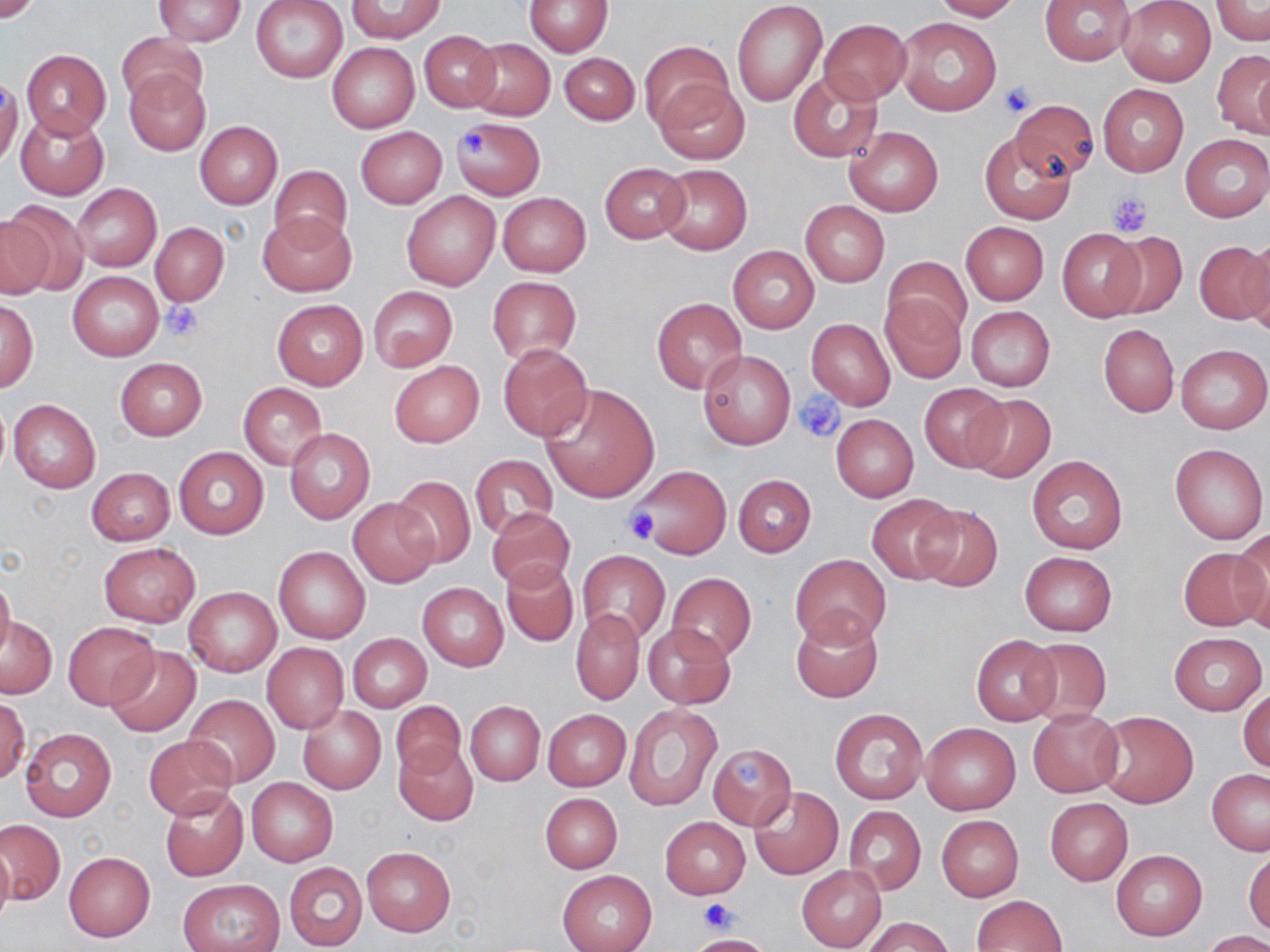
{
  "slide_level_diagnosis": "no evidence of blood parasites",
  "modality": "light microscopy",
  "image_size": "1270×952 pixels",
  "preparation": "thin blood film",
  "platelet_locations": "approximate bounding boxes as named x1/y1/x2/y2 corners in pixels: (x1=998, y1=80, x2=1038, y2=118), (x1=460, y1=130, x2=489, y2=156), (x1=1108, y1=191, x2=1153, y2=236), (x1=161, y1=300, x2=203, y2=341), (x1=796, y1=392, x2=845, y2=443), (x1=621, y1=507, x2=660, y2=546), (x1=733, y1=754, x2=761, y2=784), (x1=699, y1=898, x2=736, y2=934)",
  "uninfected_red_blood_cell_locations": "approximate bounding boxes as named x1/y1/x2/y2 corners in pixels: (x1=0, y1=0, x2=44, y2=23), (x1=251, y1=0, x2=347, y2=82), (x1=524, y1=0, x2=611, y2=56), (x1=733, y1=0, x2=828, y2=107), (x1=929, y1=0, x2=1021, y2=21), (x1=1039, y1=0, x2=1137, y2=65), (x1=153, y1=1, x2=247, y2=46), (x1=346, y1=1, x2=448, y2=42), (x1=1118, y1=1, x2=1215, y2=86), (x1=1210, y1=1, x2=1270, y2=44), (x1=895, y1=17, x2=1001, y2=117), (x1=819, y1=19, x2=911, y2=103), (x1=418, y1=30, x2=501, y2=111), (x1=116, y1=32, x2=205, y2=109), (x1=467, y1=38, x2=555, y2=121), (x1=641, y1=41, x2=732, y2=128), (x1=326, y1=42, x2=420, y2=133), (x1=1211, y1=49, x2=1270, y2=137), (x1=22, y1=50, x2=111, y2=138), (x1=560, y1=53, x2=640, y2=124), (x1=124, y1=68, x2=211, y2=156), (x1=787, y1=69, x2=884, y2=162), (x1=0, y1=75, x2=22, y2=168), (x1=654, y1=80, x2=750, y2=166), (x1=1097, y1=83, x2=1188, y2=177), (x1=1010, y1=99, x2=1099, y2=180), (x1=15, y1=110, x2=110, y2=200), (x1=450, y1=117, x2=546, y2=200), (x1=194, y1=121, x2=282, y2=208), (x1=845, y1=125, x2=943, y2=216), (x1=355, y1=126, x2=447, y2=208), (x1=980, y1=131, x2=1075, y2=224), (x1=1180, y1=134, x2=1270, y2=222), (x1=599, y1=162, x2=690, y2=243), (x1=657, y1=164, x2=751, y2=255), (x1=269, y1=165, x2=352, y2=247), (x1=73, y1=184, x2=161, y2=272), (x1=401, y1=191, x2=500, y2=290), (x1=497, y1=192, x2=591, y2=277), (x1=0, y1=199, x2=90, y2=295), (x1=800, y1=200, x2=889, y2=287), (x1=259, y1=210, x2=355, y2=295), (x1=960, y1=221, x2=1049, y2=304), (x1=151, y1=223, x2=229, y2=306), (x1=1056, y1=229, x2=1145, y2=321), (x1=1105, y1=231, x2=1187, y2=319), (x1=1246, y1=231, x2=1270, y2=332), (x1=1194, y1=238, x2=1270, y2=326), (x1=728, y1=246, x2=818, y2=332), (x1=882, y1=256, x2=970, y2=344), (x1=68, y1=272, x2=164, y2=360), (x1=488, y1=277, x2=582, y2=364), (x1=368, y1=286, x2=458, y2=373), (x1=880, y1=294, x2=966, y2=382), (x1=651, y1=297, x2=747, y2=393), (x1=1, y1=298, x2=38, y2=393), (x1=272, y1=299, x2=368, y2=390), (x1=965, y1=307, x2=1055, y2=391), (x1=807, y1=317, x2=897, y2=410), (x1=1099, y1=324, x2=1178, y2=417), (x1=498, y1=342, x2=592, y2=442), (x1=1176, y1=343, x2=1269, y2=435), (x1=698, y1=350, x2=795, y2=450), (x1=115, y1=358, x2=206, y2=440), (x1=389, y1=360, x2=484, y2=448), (x1=239, y1=383, x2=327, y2=469), (x1=918, y1=383, x2=1012, y2=471), (x1=539, y1=384, x2=659, y2=503), (x1=965, y1=393, x2=1055, y2=479), (x1=9, y1=399, x2=101, y2=494), (x1=831, y1=414, x2=918, y2=501), (x1=284, y1=429, x2=374, y2=522), (x1=1170, y1=443, x2=1267, y2=544), (x1=174, y1=447, x2=268, y2=538), (x1=469, y1=455, x2=558, y2=540), (x1=1028, y1=455, x2=1128, y2=554), (x1=632, y1=465, x2=730, y2=559), (x1=87, y1=467, x2=174, y2=545), (x1=732, y1=474, x2=817, y2=556), (x1=391, y1=477, x2=476, y2=570), (x1=866, y1=495, x2=962, y2=583), (x1=348, y1=498, x2=439, y2=587), (x1=911, y1=501, x2=1004, y2=592), (x1=486, y1=507, x2=576, y2=591), (x1=1230, y1=530, x2=1270, y2=628), (x1=99, y1=543, x2=200, y2=626), (x1=273, y1=545, x2=371, y2=643), (x1=1177, y1=547, x2=1264, y2=631), (x1=576, y1=550, x2=670, y2=646), (x1=1018, y1=552, x2=1117, y2=636), (x1=790, y1=554, x2=889, y2=647), (x1=499, y1=559, x2=579, y2=647), (x1=0, y1=572, x2=15, y2=663), (x1=667, y1=573, x2=757, y2=662), (x1=419, y1=582, x2=508, y2=671), (x1=184, y1=587, x2=281, y2=676), (x1=571, y1=608, x2=644, y2=704), (x1=790, y1=610, x2=883, y2=703), (x1=1, y1=617, x2=56, y2=698), (x1=63, y1=624, x2=160, y2=708), (x1=642, y1=624, x2=735, y2=709), (x1=1168, y1=631, x2=1266, y2=715), (x1=347, y1=633, x2=431, y2=711), (x1=972, y1=634, x2=1060, y2=725), (x1=1024, y1=638, x2=1110, y2=722), (x1=262, y1=642, x2=348, y2=733), (x1=106, y1=646, x2=201, y2=736), (x1=1238, y1=688, x2=1270, y2=773), (x1=183, y1=694, x2=279, y2=787), (x1=1, y1=698, x2=28, y2=784), (x1=390, y1=700, x2=465, y2=781), (x1=466, y1=701, x2=544, y2=786), (x1=625, y1=704, x2=722, y2=811), (x1=298, y1=706, x2=385, y2=794), (x1=829, y1=707, x2=929, y2=805), (x1=1028, y1=708, x2=1123, y2=797), (x1=542, y1=710, x2=631, y2=791), (x1=1095, y1=711, x2=1199, y2=808), (x1=921, y1=722, x2=1020, y2=815), (x1=20, y1=726, x2=116, y2=822), (x1=145, y1=735, x2=237, y2=818), (x1=394, y1=741, x2=479, y2=826), (x1=707, y1=743, x2=798, y2=828), (x1=1206, y1=770, x2=1270, y2=855), (x1=246, y1=777, x2=338, y2=866), (x1=159, y1=786, x2=249, y2=882), (x1=749, y1=787, x2=843, y2=879), (x1=540, y1=792, x2=623, y2=872), (x1=1045, y1=798, x2=1133, y2=885), (x1=843, y1=806, x2=926, y2=896), (x1=661, y1=816, x2=749, y2=898), (x1=937, y1=816, x2=1023, y2=901), (x1=0, y1=817, x2=65, y2=905), (x1=0, y1=839, x2=14, y2=929), (x1=363, y1=848, x2=455, y2=936), (x1=1244, y1=848, x2=1269, y2=937), (x1=1111, y1=849, x2=1207, y2=941), (x1=63, y1=852, x2=155, y2=942), (x1=284, y1=862, x2=368, y2=951), (x1=797, y1=865, x2=887, y2=952), (x1=557, y1=870, x2=657, y2=952), (x1=178, y1=880, x2=285, y2=952), (x1=972, y1=895, x2=1067, y2=951), (x1=862, y1=916, x2=952, y2=952), (x1=1203, y1=931, x2=1270, y2=952), (x1=686, y1=934, x2=776, y2=952)",
  "magnification": "1000x",
  "stain": "May-Grünwald-Giemsa",
  "field_of_view": "single"
}